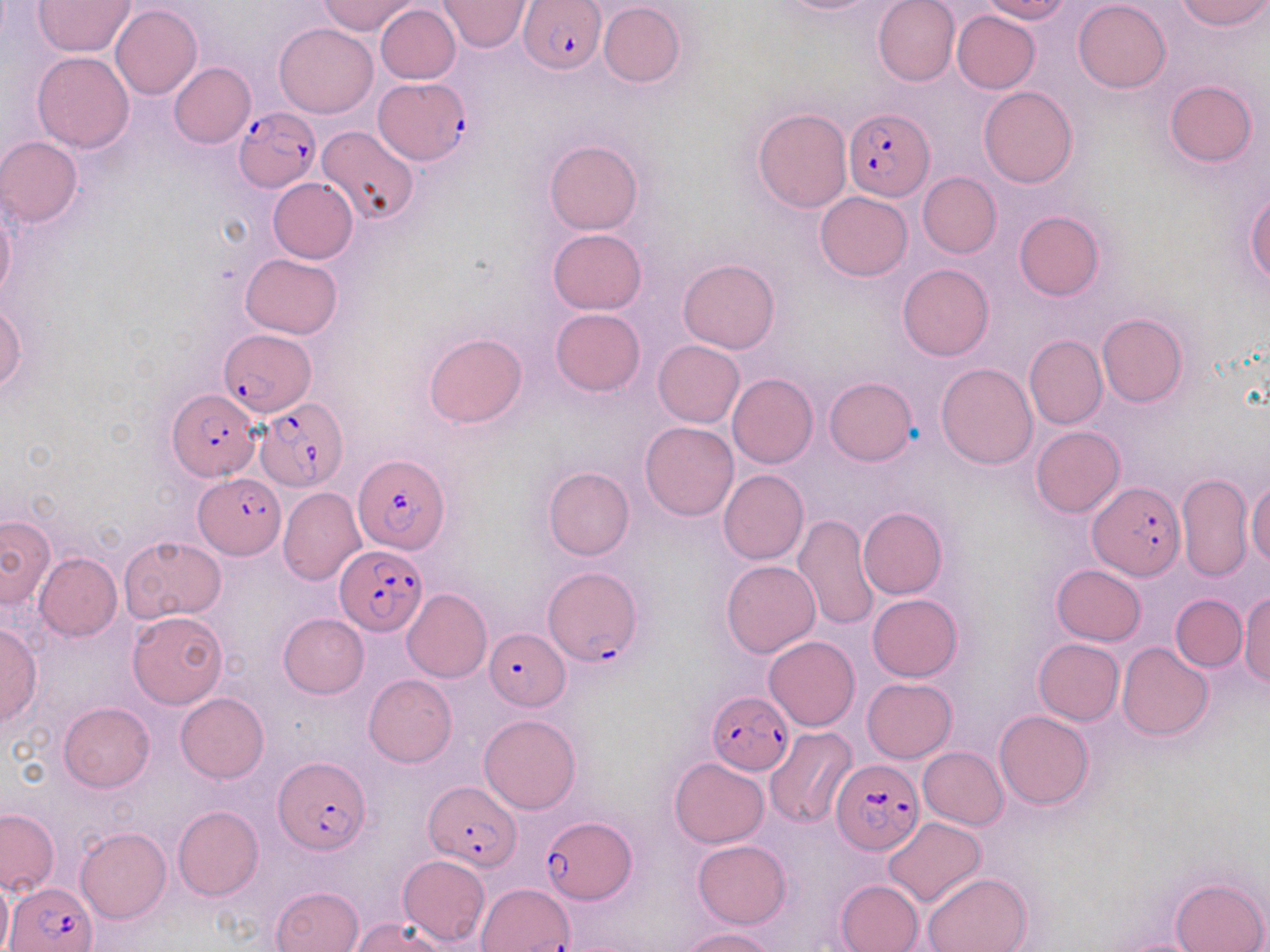

slide-level diagnosis = Plasmodium falciparum
stain = May-Grünwald-Giemsa
field of view = one of a larger specimen
uninfected red blood cell locations = approximate bounding boxes as (x1,y1)-(x2,y2) corner pairs in pixels: (318,0)-(421,35), (769,0)-(888,15), (873,0)-(960,86), (978,0)-(1070,23), (1073,0)-(1171,92), (1175,0)-(1268,31), (33,1)-(136,56), (440,1)-(529,52), (597,2)-(684,88), (110,4)-(203,99), (374,4)-(460,83), (952,10)-(1040,93), (274,23)-(377,118), (32,51)-(135,152), (168,62)-(255,148), (1164,79)-(1257,166), (978,86)-(1077,187), (752,107)-(853,214), (316,125)-(419,226), (2,136)-(83,225), (544,140)-(641,235), (917,172)-(1001,258), (268,177)-(359,263), (814,191)-(911,281), (1245,191)-(1270,284), (1,201)-(15,302), (1013,210)-(1105,300), (547,229)-(647,315), (240,252)-(343,339), (678,258)-(779,353), (897,263)-(994,360), (0,302)-(27,393), (551,309)-(646,396), (1097,312)-(1187,407), (424,333)-(528,429), (1024,334)-(1107,429), (653,340)-(744,428), (937,362)-(1038,469), (727,372)-(818,468), (824,377)-(917,465), (640,421)-(739,520), (1030,426)-(1124,517), (542,466)-(635,560), (719,470)-(809,565), (1177,473)-(1253,580), (1247,480)-(1270,565), (278,488)-(367,586), (858,505)-(947,599), (0,513)-(56,609), (794,514)-(879,632), (119,536)-(225,623), (34,553)-(122,641), (721,560)-(820,657), (1051,565)-(1145,646), (402,588)-(492,683), (1238,592)-(1269,688), (868,594)-(962,681), (1171,594)-(1247,671), (128,611)-(227,709), (278,613)-(368,697), (0,624)-(41,727), (764,635)-(859,731), (1034,638)-(1124,723), (1117,642)-(1213,741), (364,675)-(456,767), (862,678)-(956,763), (176,693)-(269,782), (58,702)-(154,791), (994,709)-(1093,809), (479,714)-(580,814), (765,727)-(856,829), (918,746)-(1008,829), (669,757)-(769,848), (173,806)-(263,901), (0,808)-(59,895), (883,816)-(985,906), (75,827)-(171,923), (692,839)-(791,928), (397,855)-(489,946), (922,872)-(1032,952), (1170,876)-(1267,952), (0,877)-(12,952), (835,879)-(923,952), (271,885)-(363,952), (350,918)-(445,951), (678,927)-(776,951)
Plasmodium falciparum-infected red blood cell locations = approximate bounding boxes as (x1,y1)-(x2,y2) corner pairs in pixels: (519,0)-(606,73), (376,78)-(469,166), (233,107)-(320,193), (842,108)-(934,201), (220,330)-(314,416), (168,390)-(259,479), (254,396)-(346,492), (354,453)-(448,553), (194,475)-(283,558), (1089,481)-(1183,581), (334,545)-(427,634), (541,566)-(642,667), (486,629)-(569,710), (707,693)-(792,776), (273,756)-(370,855), (831,759)-(924,855), (424,783)-(519,869), (542,815)-(635,905), (5,881)-(96,952), (479,883)-(576,950)
preparation = thin blood film
magnification = 1000x
image size = 1270×952 pixels
modality = light microscopy